Assess this cell for malaria.
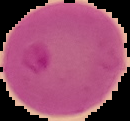
It is parasitized.

Summary:
  - Image size: 130×121 pixels
  - Image type: segmented cell region with the area outside set to black
  - Preparation: thin blood film